Comment on the morphology of the erythrocytes.
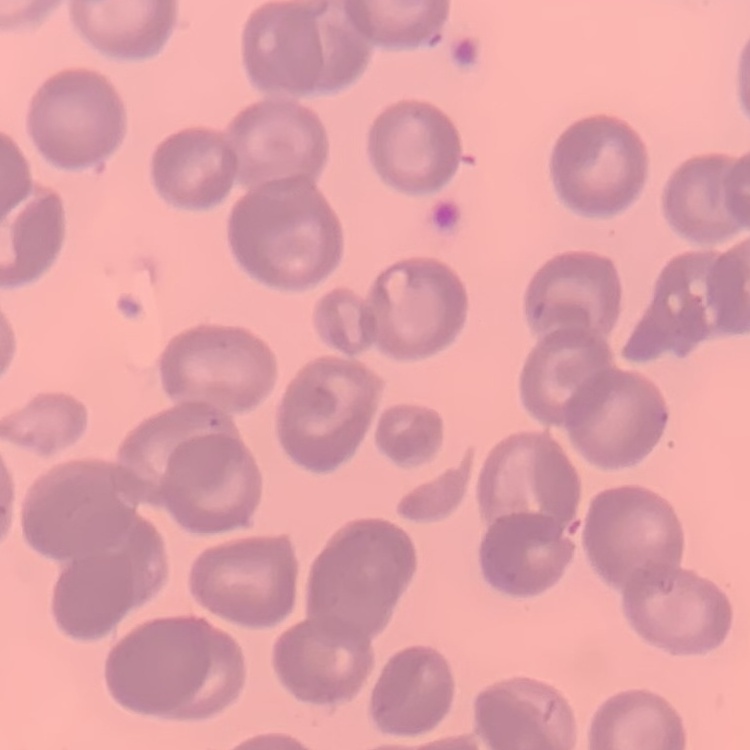

No rouleaux formation.

Square crop of a larger photomicrograph. Stained with either Field's or Giemsa. Thin peripheral smear.